Assess this cell for malaria.
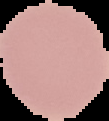

Uninfected.

image type = segmented cell region with the area outside set to black
image size = 109×121 pixels
preparation = thin blood smear